Outline each Plasmodium falciparum-infected red blood cell.
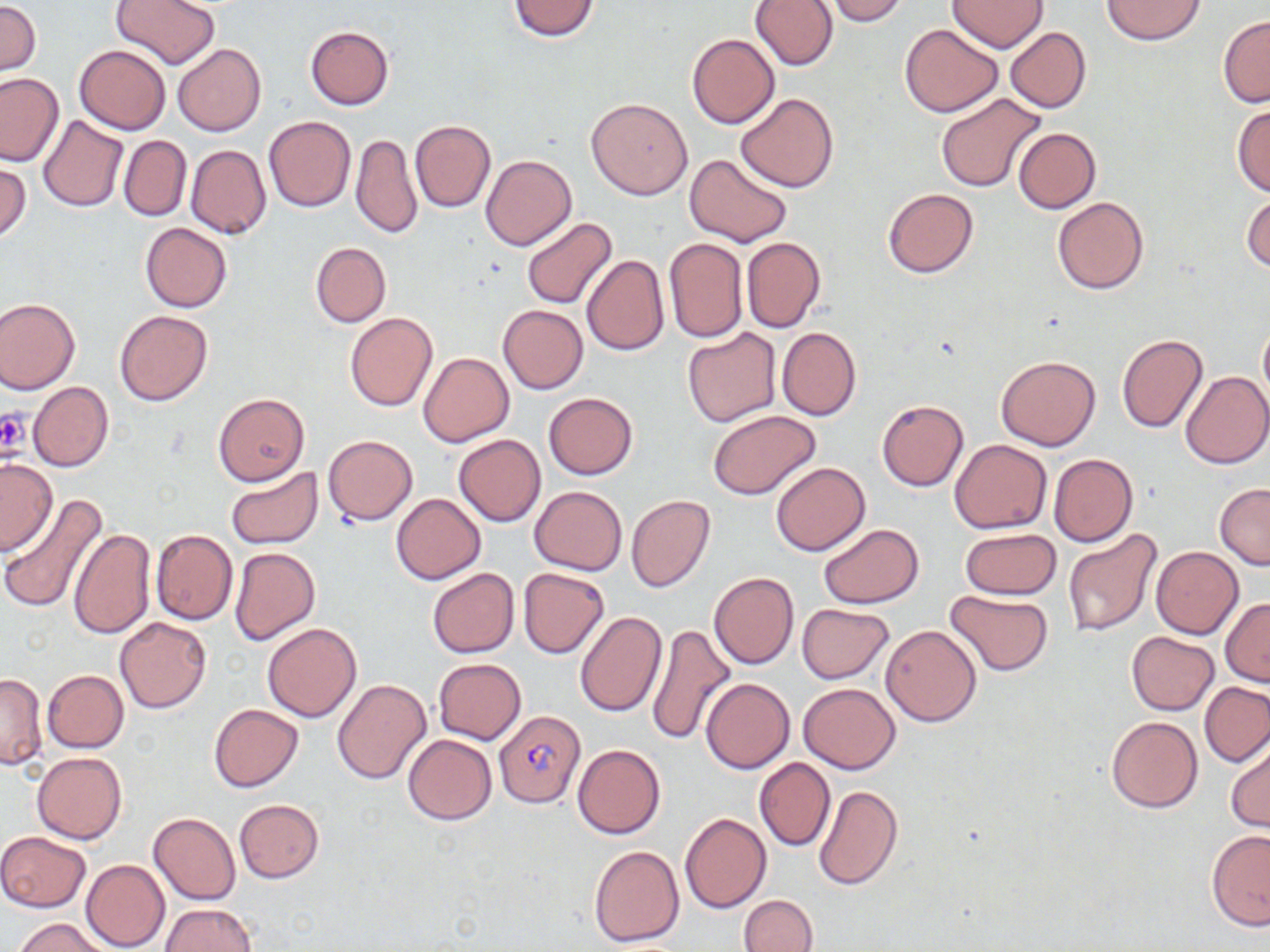

Approximate bounding boxes as named x1/y1/x2/y2 corners in pixels.
Plasmodium falciparum-infected red blood cells: (x1=493, y1=708, x2=586, y2=807).

slide-level diagnosis = Plasmodium falciparum
uninfected red blood cell locations = approximate bounding boxes as named x1/y1/x2/y2 corners in pixels: (x1=110, y1=0, x2=219, y2=69), (x1=751, y1=0, x2=837, y2=71), (x1=822, y1=0, x2=909, y2=25), (x1=1100, y1=0, x2=1207, y2=45), (x1=508, y1=1, x2=600, y2=41), (x1=947, y1=1, x2=1047, y2=52), (x1=0, y1=2, x2=40, y2=74), (x1=1217, y1=16, x2=1270, y2=108), (x1=899, y1=24, x2=1003, y2=117), (x1=305, y1=25, x2=393, y2=109), (x1=1005, y1=27, x2=1092, y2=113), (x1=687, y1=34, x2=779, y2=128), (x1=172, y1=43, x2=266, y2=136), (x1=73, y1=45, x2=171, y2=134), (x1=0, y1=73, x2=64, y2=166), (x1=736, y1=92, x2=838, y2=192), (x1=936, y1=93, x2=1047, y2=195), (x1=586, y1=98, x2=692, y2=199), (x1=1232, y1=103, x2=1270, y2=196), (x1=39, y1=115, x2=127, y2=212), (x1=263, y1=116, x2=355, y2=212), (x1=409, y1=120, x2=495, y2=211), (x1=1012, y1=127, x2=1100, y2=213), (x1=351, y1=133, x2=421, y2=239), (x1=119, y1=136, x2=191, y2=220), (x1=186, y1=145, x2=271, y2=240), (x1=685, y1=153, x2=793, y2=247), (x1=481, y1=154, x2=576, y2=250), (x1=0, y1=162, x2=31, y2=241), (x1=883, y1=188, x2=979, y2=276), (x1=1242, y1=191, x2=1270, y2=275), (x1=1052, y1=197, x2=1148, y2=294), (x1=521, y1=217, x2=618, y2=310), (x1=140, y1=223, x2=232, y2=312), (x1=741, y1=237, x2=826, y2=334), (x1=664, y1=238, x2=748, y2=342), (x1=311, y1=243, x2=390, y2=327), (x1=581, y1=255, x2=668, y2=356), (x1=0, y1=296, x2=80, y2=394), (x1=498, y1=305, x2=587, y2=394), (x1=114, y1=310, x2=212, y2=406), (x1=344, y1=312, x2=437, y2=411), (x1=1259, y1=318, x2=1270, y2=411), (x1=777, y1=327, x2=861, y2=420), (x1=682, y1=328, x2=783, y2=427), (x1=1116, y1=334, x2=1208, y2=432), (x1=419, y1=352, x2=514, y2=447), (x1=996, y1=356, x2=1100, y2=451), (x1=1181, y1=370, x2=1270, y2=468), (x1=28, y1=381, x2=113, y2=472), (x1=543, y1=392, x2=638, y2=480), (x1=213, y1=393, x2=309, y2=485), (x1=877, y1=400, x2=968, y2=491), (x1=708, y1=410, x2=821, y2=500), (x1=453, y1=434, x2=546, y2=527), (x1=323, y1=435, x2=417, y2=525), (x1=949, y1=439, x2=1052, y2=534), (x1=1048, y1=454, x2=1139, y2=548), (x1=0, y1=457, x2=57, y2=555), (x1=770, y1=462, x2=870, y2=556), (x1=226, y1=467, x2=323, y2=549), (x1=1215, y1=483, x2=1270, y2=570), (x1=530, y1=486, x2=627, y2=574), (x1=391, y1=493, x2=485, y2=584), (x1=626, y1=494, x2=715, y2=592), (x1=1, y1=495, x2=108, y2=613), (x1=818, y1=523, x2=922, y2=609), (x1=1062, y1=526, x2=1163, y2=638), (x1=151, y1=528, x2=237, y2=625), (x1=961, y1=528, x2=1061, y2=600), (x1=68, y1=529, x2=155, y2=640), (x1=1151, y1=546, x2=1243, y2=638), (x1=229, y1=547, x2=321, y2=646), (x1=517, y1=567, x2=609, y2=659), (x1=427, y1=568, x2=518, y2=658), (x1=709, y1=572, x2=799, y2=670), (x1=946, y1=590, x2=1053, y2=676), (x1=1220, y1=597, x2=1270, y2=685), (x1=797, y1=603, x2=895, y2=683), (x1=576, y1=611, x2=667, y2=717), (x1=115, y1=616, x2=212, y2=712), (x1=262, y1=621, x2=362, y2=722), (x1=645, y1=623, x2=737, y2=744), (x1=879, y1=623, x2=981, y2=726), (x1=1125, y1=631, x2=1220, y2=715), (x1=433, y1=658, x2=526, y2=745), (x1=42, y1=669, x2=128, y2=752), (x1=0, y1=672, x2=46, y2=769), (x1=701, y1=677, x2=795, y2=774), (x1=332, y1=678, x2=432, y2=784), (x1=798, y1=682, x2=900, y2=773), (x1=1201, y1=682, x2=1269, y2=766), (x1=208, y1=704, x2=303, y2=791), (x1=1105, y1=716, x2=1203, y2=813), (x1=404, y1=734, x2=496, y2=824), (x1=1226, y1=737, x2=1270, y2=833), (x1=572, y1=744, x2=666, y2=839), (x1=32, y1=752, x2=126, y2=844), (x1=754, y1=758, x2=835, y2=850), (x1=813, y1=784, x2=903, y2=891), (x1=235, y1=799, x2=323, y2=881), (x1=679, y1=812, x2=772, y2=914), (x1=149, y1=813, x2=240, y2=906), (x1=1206, y1=830, x2=1270, y2=929), (x1=0, y1=831, x2=90, y2=913), (x1=589, y1=844, x2=684, y2=947), (x1=81, y1=859, x2=170, y2=951), (x1=738, y1=894, x2=818, y2=952), (x1=159, y1=904, x2=257, y2=952), (x1=15, y1=917, x2=110, y2=952)
preparation = thin blood film
field of view = single
image size = 1270×952 pixels
magnification = 1000x
platelet locations = approximate bounding boxes as named x1/y1/x2/y2 corners in pixels: (x1=0, y1=408, x2=29, y2=458)
stain = May-Grünwald-Giemsa
modality = light microscopy